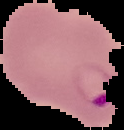

image size = 124×130 pixels
result = malaria parasites detected
image type = segmented cell region on a black background
preparation = thin blood film